Classify this cell by malaria status.
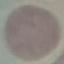
Uninfected.

Giemsa stain. Automatically extracted cell patch, resized to 64 × 64 pixels. Acquired by smartphone through the microscope eyepiece. Thin smear of blood.